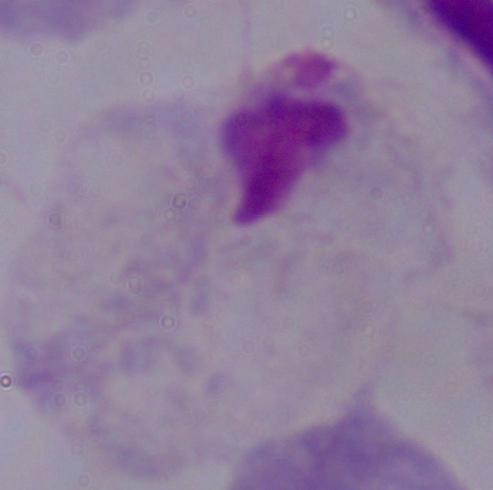
Summary:
  - Identification: trichomonad
  - Magnification: 1000x
  - Modality: micrograph